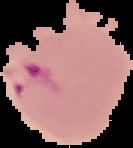

Cell region segmented out of the field of view; the surrounding area is masked to black. From a thin blood smear. Malaria status: parasitized. Image is 133×148 pixels.